Report the malaria status of this cell.
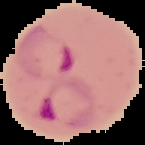

It is parasitized.

image type = segmented cell region with the area outside set to black
image size = 145×145 pixels
preparation = thin blood smear